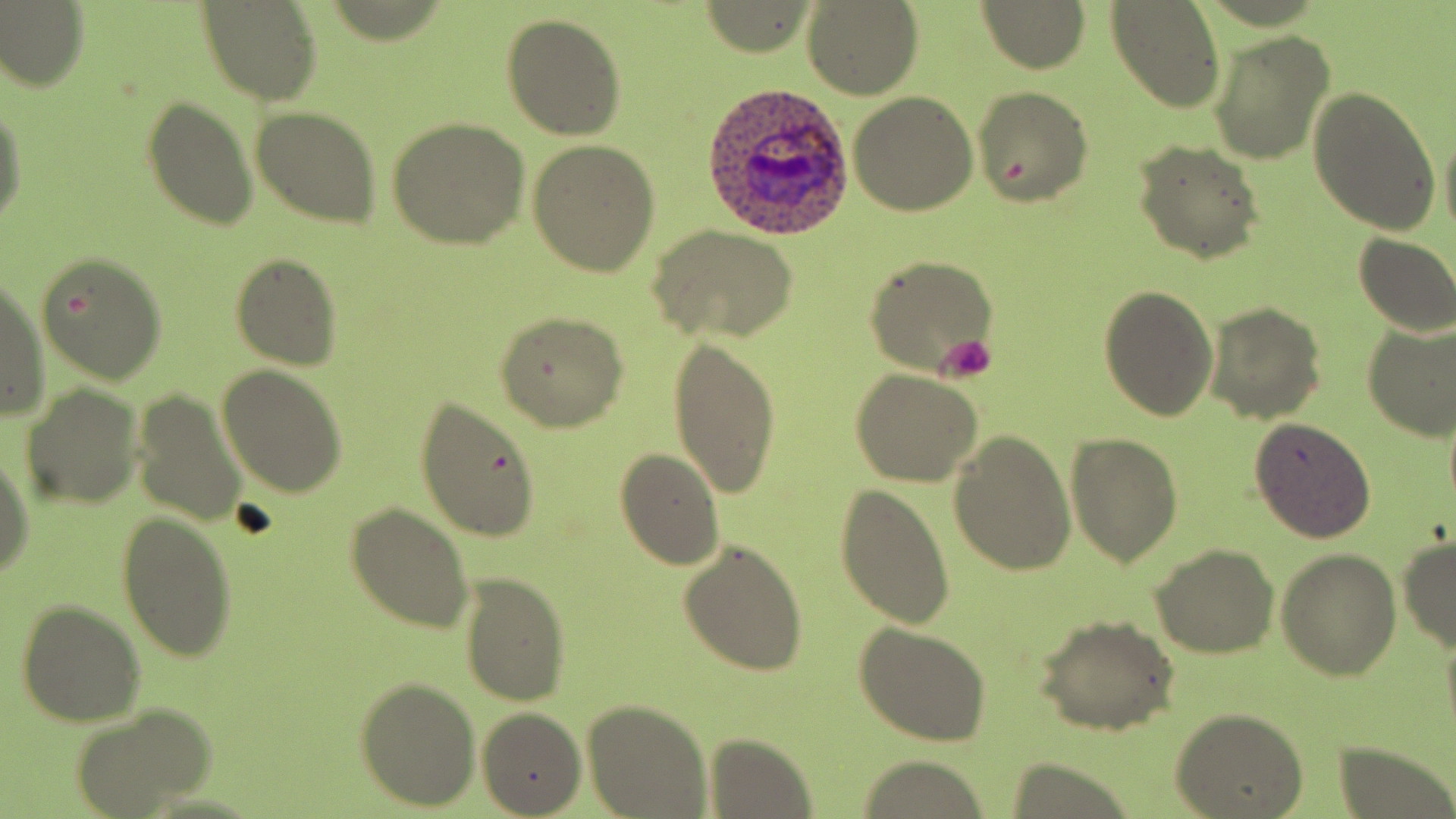
slide-level diagnosis = Plasmodium ovale
platelet locations = approximate bounding boxes as (x1,y1)-(x2,y2) corner pairs in pixels: (937,333)-(997,382)
field of view = one of a larger specimen
image size = 1456×819 pixels
preparation = thin blood smear
uninfected red blood cell locations = approximate bounding boxes as (x1,y1)-(x2,y2) corner pairs in pixels: (0,2)-(88,94), (978,2)-(1089,72), (1105,2)-(1227,111), (197,3)-(322,106), (801,3)-(922,98), (502,13)-(626,141), (1209,29)-(1334,163), (971,86)-(1094,206), (1307,87)-(1443,235), (848,90)-(979,216), (142,97)-(260,232), (0,101)-(25,227), (250,106)-(383,228), (1438,112)-(1456,250), (388,117)-(529,249), (528,137)-(660,275), (1133,142)-(1264,262), (647,224)-(798,345), (1352,233)-(1456,336), (32,250)-(167,383), (230,254)-(341,370), (864,255)-(998,376), (0,272)-(48,422), (1099,283)-(1217,420), (1205,302)-(1325,423), (494,310)-(629,431), (1361,320)-(1456,440), (666,335)-(781,502), (217,365)-(348,499), (851,369)-(983,486), (19,383)-(144,510), (130,389)-(249,528), (416,397)-(543,542), (1249,416)-(1376,542), (1064,430)-(1182,567), (949,431)-(1077,575), (0,441)-(33,581), (615,448)-(723,571), (833,484)-(955,628), (345,502)-(472,631), (115,510)-(237,664), (1398,537)-(1456,654), (678,542)-(808,675), (1151,546)-(1278,659), (1276,550)-(1402,681), (460,572)-(569,706), (16,599)-(147,726), (1037,617)-(1178,734), (854,624)-(991,746), (356,678)-(480,811), (582,700)-(712,819), (71,705)-(213,819), (478,708)-(586,817), (1175,708)-(1307,818), (702,732)-(817,817), (1331,742)-(1454,819), (853,758)-(996,816), (1004,758)-(1137,819)
modality = light microscopy
magnification = 1000x
stain = May-Grünwald-Giemsa
Plasmodium ovale-infected red blood cell locations = approximate bounding boxes as (x1,y1)-(x2,y2) corner pairs in pixels: (698,84)-(856,241)